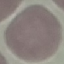 Malaria status: uninfected. Thin smear of blood. Giemsa stain. Automatically extracted cell patch, resized to 64 × 64 pixels. Photographed with a smartphone camera at the microscope eyepiece.